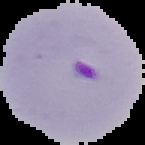

Image is 145×145 pixels. Result: Plasmodium parasites detected. From a thin blood film. The area outside the segmented cell region is set to black.